Comment on the morphology of the red blood cells.
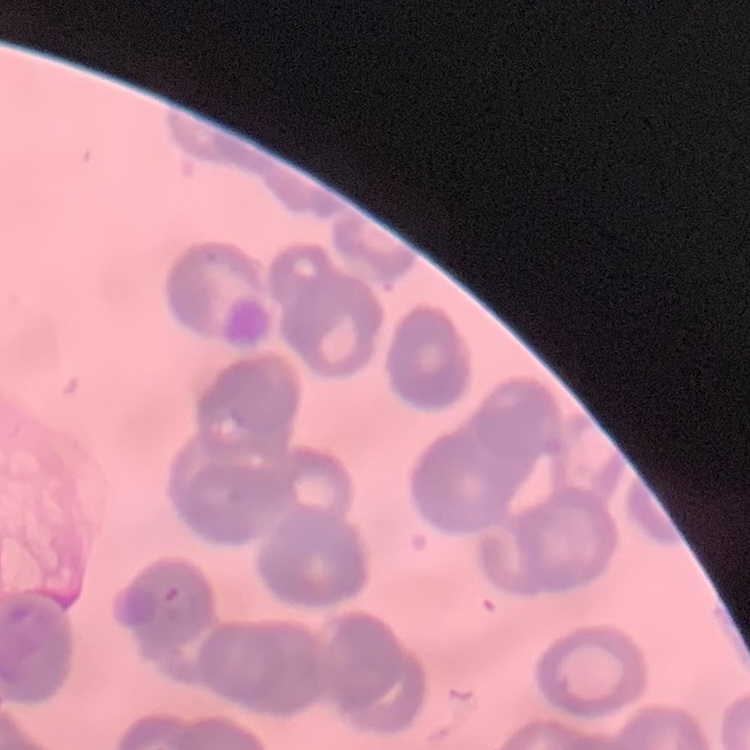

They show rouleaux formation.

stain: Field's or Giemsa
preparation: thin blood film
image_type: square crop of a larger photomicrograph